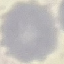
Malaria status: uninfected. Thin smear of blood. Photographed with a smartphone camera at the microscope eyepiece. Giemsa stain. Automatically extracted cell patch, resized to 64 × 64 pixels.